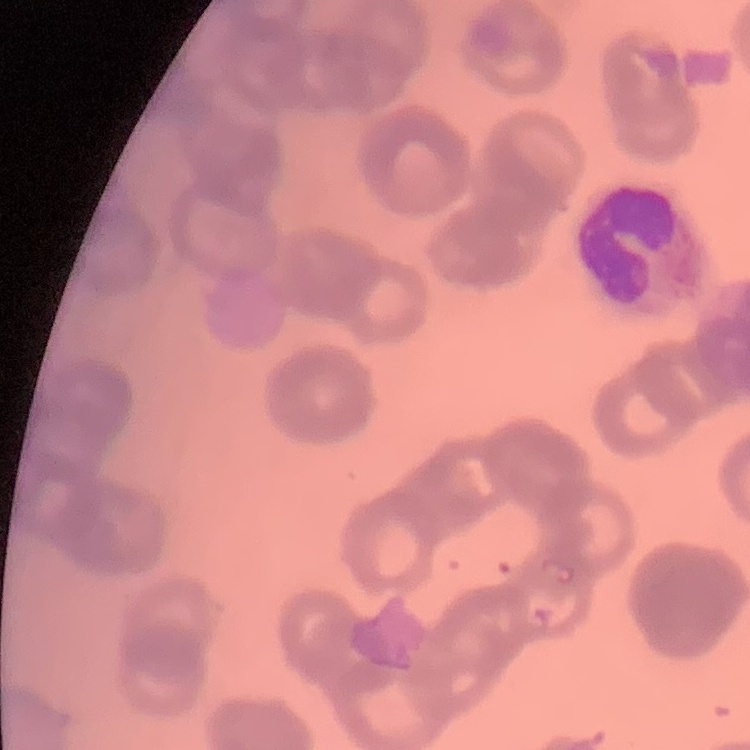
red blood cell morphology = rouleaux formation
preparation = thin blood smear
image type = one tile cut from a larger photomicrograph
stain = Field's or Giemsa